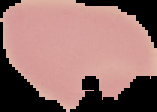

From a thin blood film. Image is 157×112 pixels. Malaria status: uninfected. Cell region segmented out of the field of view; the surrounding area is masked to black.